Find the cells and give the type of each one.
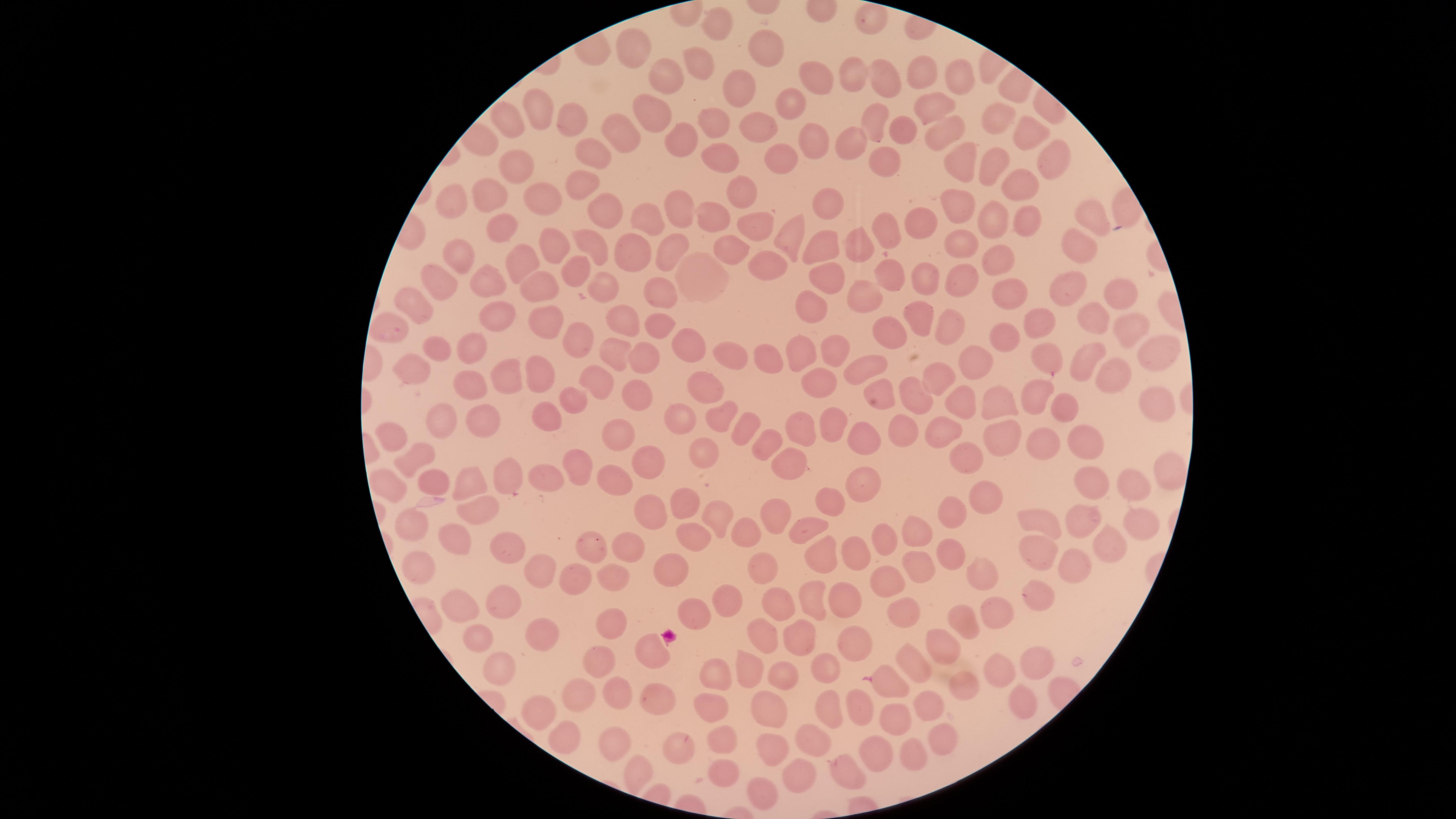

No parasitized RBCs identified.
Approximate marker points as [x, y] in pixels.
Uninfected RBCs: [718, 20], [767, 47], [629, 48], [699, 63], [660, 74], [884, 74], [954, 74], [848, 76], [816, 78], [923, 80], [742, 85], [790, 105], [927, 106], [649, 110], [537, 112], [569, 114], [997, 120], [872, 121], [507, 122], [714, 123], [941, 129], [615, 131], [766, 132], [899, 133], [1024, 134], [681, 139], [813, 145], [850, 146], [598, 155], [780, 156], [723, 158], [960, 159], [991, 162], [1062, 162], [887, 167], [519, 172], [583, 180], [1020, 183], [737, 189], [489, 200], [826, 202], [545, 203], [953, 204], [453, 207], [672, 207], [604, 212], [1022, 215], [1086, 216], [712, 218], [995, 218], [918, 221], [652, 222], [758, 225], [887, 227], [788, 228], [507, 230], [551, 242], [826, 244], [1086, 244], [859, 245], [962, 245], [665, 248], [589, 249], [458, 254], [628, 254], [732, 255], [530, 261], [766, 262], [1005, 263], [576, 276], [924, 277], [490, 278], [821, 279], [887, 281], [956, 282], [438, 283], [605, 283], [1068, 286], [539, 288], [1005, 293], [1121, 294], [664, 297], [869, 299], [415, 302], [811, 308], [498, 316], [629, 316], [920, 316], [1091, 318], [546, 319], [1040, 325], [948, 326], [658, 329], [386, 332], [1006, 333], [1125, 334], [571, 337], [892, 337], [695, 346], [436, 347], [831, 348], [476, 350], [805, 350], [1156, 350], [609, 352], [727, 353], [645, 355], [1047, 355], [773, 357], [1083, 358], [970, 360], [870, 365], [409, 369], [931, 371], [502, 372], [541, 373], [1105, 375], [590, 382], [472, 383], [712, 383], [819, 383], [958, 393], [879, 395], [903, 396], [637, 398], [1037, 398], [569, 399], [1150, 401], [1068, 402], [1003, 404], [677, 416], [724, 416], [835, 416], [544, 418], [450, 419], [489, 420], [746, 426], [801, 429], [943, 429], [899, 431], [862, 434], [624, 435], [1004, 437], [382, 439], [1044, 442], [1084, 444], [763, 447], [703, 450], [969, 453], [414, 457], [574, 458], [654, 462], [789, 466], [1169, 468], [462, 476], [614, 476], [436, 478], [510, 479], [540, 482], [859, 483], [1093, 484], [1122, 486], [388, 487], [831, 498], [978, 500], [478, 504], [679, 506], [653, 511], [1081, 511], [773, 513], [1133, 516], [716, 517], [952, 517], [408, 523], [1039, 523], [748, 530], [810, 531], [916, 534], [692, 535], [452, 537], [883, 537], [1099, 537], [626, 545], [501, 547], [596, 547], [1034, 550], [854, 551], [951, 553], [819, 558], [535, 565], [761, 566], [910, 567], [416, 569], [1070, 569], [672, 570], [968, 572], [622, 576], [571, 578], [883, 583], [818, 591], [1039, 592], [852, 599], [498, 601], [727, 601], [461, 602], [999, 610], [694, 611], [785, 612], [904, 612], [966, 622], [614, 624], [546, 632], [479, 635], [767, 635], [799, 638], [857, 642], [943, 642], [597, 652], [653, 652], [915, 659], [1035, 662], [744, 666], [819, 666], [499, 670], [998, 674], [787, 678], [710, 679], [893, 682], [956, 682], [576, 690], [613, 692], [655, 697], [827, 702], [924, 703], [1023, 703], [859, 704], [706, 707], [769, 709], [537, 713], [895, 716], [610, 737], [727, 738], [943, 738], [811, 739], [555, 740], [883, 743], [673, 747], [771, 751], [908, 757], [629, 765], [852, 765], [718, 770], [802, 771], [756, 790].
No WBCs identified.

image size = 1456×819 pixels
capture = smartphone photograph through the microscope eyepiece
stain = Giemsa
field of view = single
preparation = thin blood film
visible region = circular